Identify the preparation type.
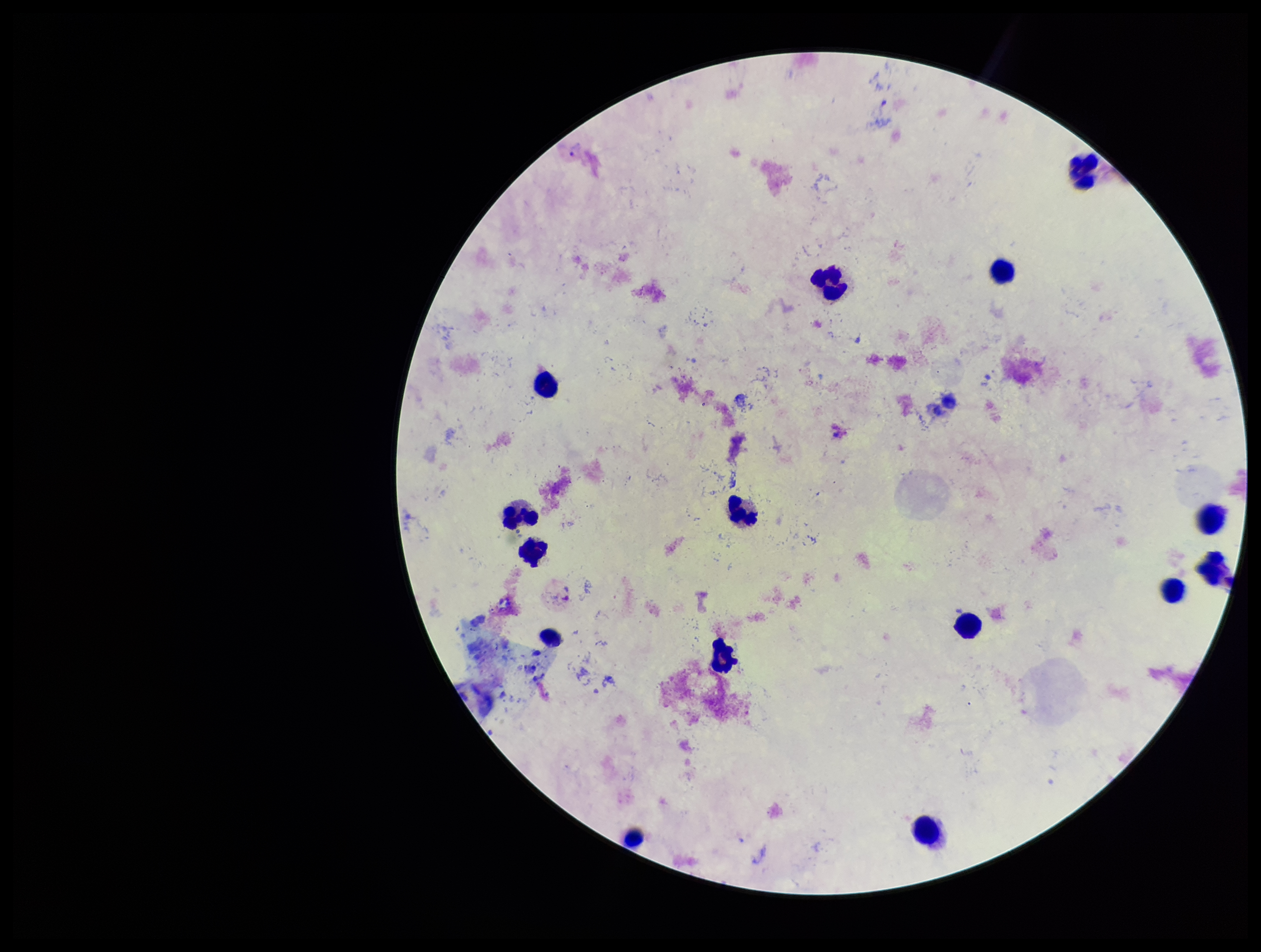
Thick.

plasmodium_parasites: identified
species_reported_for_this_patient: Plasmodium vivax
field_of_view: one from this slide
image_size: 1261×952 pixels
parasite_count: 1
leukocyte_count: 15
capture: smartphone photograph through the microscope eyepiece
stain: Giemsa
patient_malaria_status: infected